State which parasite is depicted.
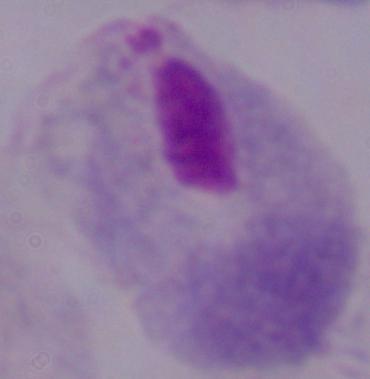
This is a trichomonad.

{
  "modality": "photomicrograph",
  "magnification": "1000x"
}